Assess for parasitized red blood cells.
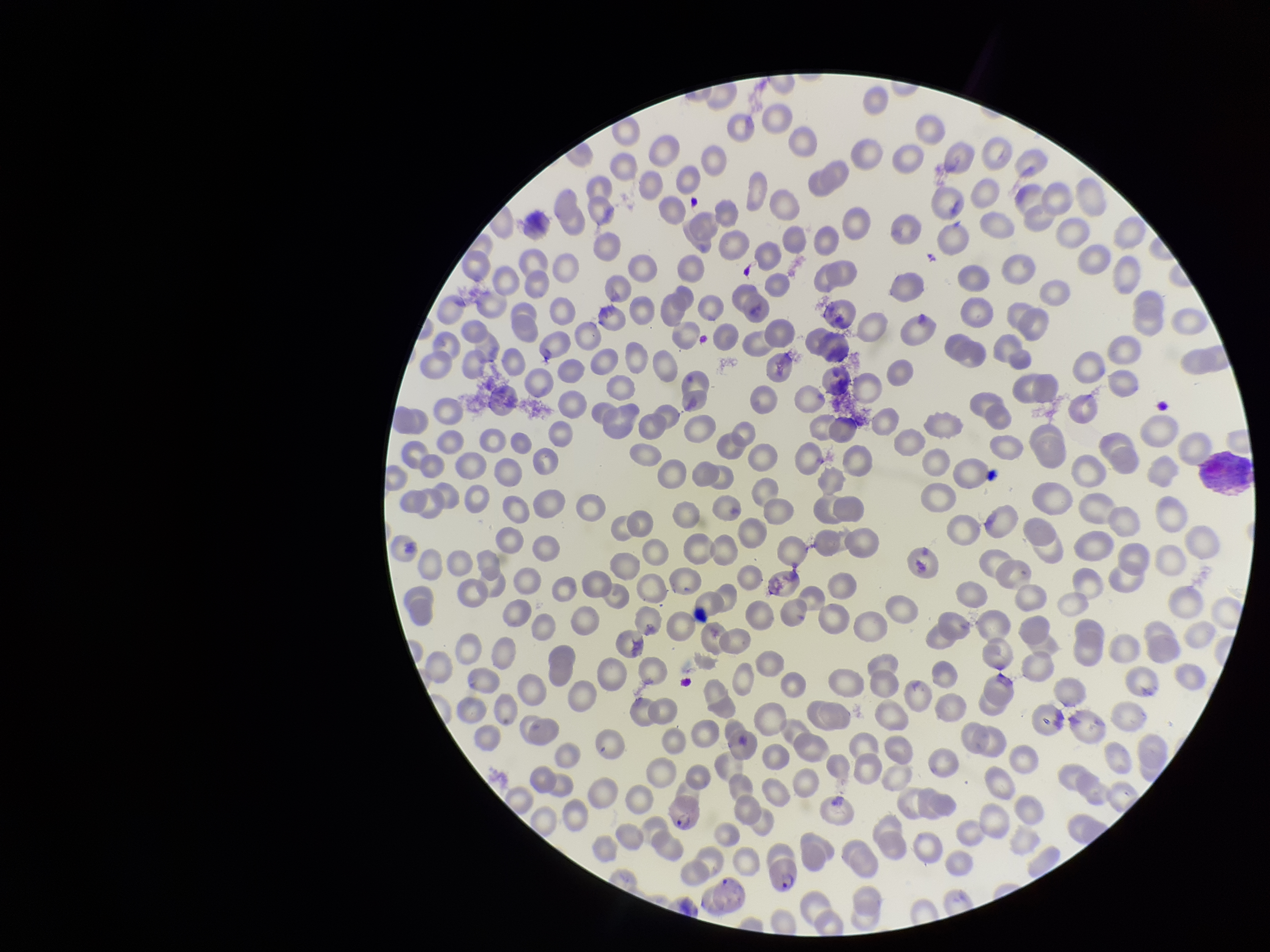

Detected.

Red blood cell count: 286. Preparation: thin. Image is 1270×952 pixels. Patient malaria status: positive. Giemsa stain. Parasitized red blood cell count: 2. Species reported for this patient: Plasmodium vivax. Photographed through the microscope eyepiece with a smartphone camera. Single field of view.